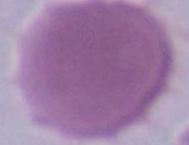

modality = micrograph
magnification = 1000x
identification = erythrocyte